Outline platelets.
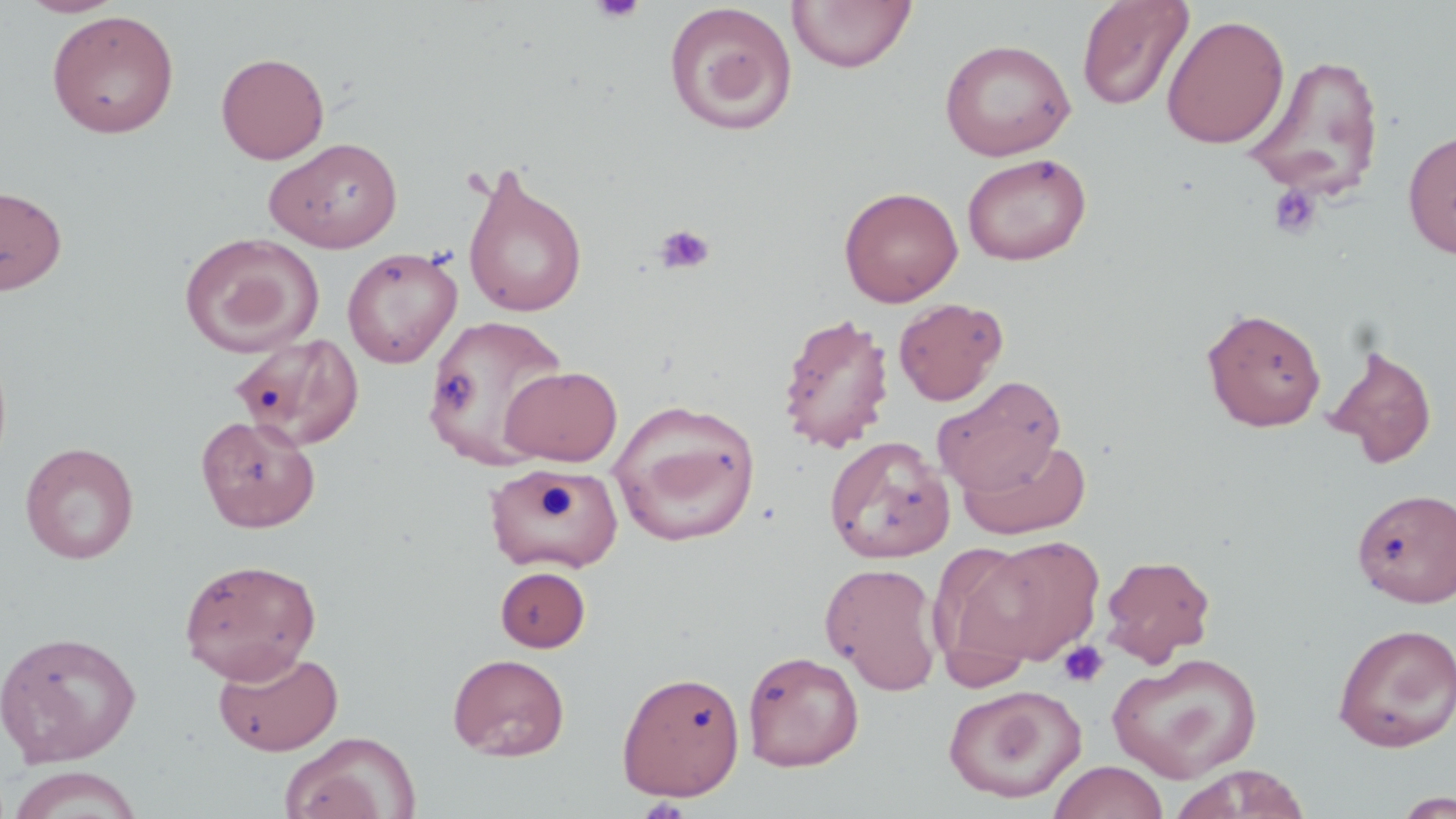

Approximate bounding boxes as [x1, y1, x2, y2] in pixels.
Platelets: [591, 0, 646, 24], [1267, 183, 1323, 240], [653, 223, 715, 275], [1058, 640, 1109, 689].

slide-level diagnosis = no evidence of blood parasites
magnification = 1000x
preparation = thin blood smear
field of view = single
image size = 1456×819 pixels
stain = May-Grünwald-Giemsa
modality = light microscopy
uninfected red blood cell locations = approximate bounding boxes as [x1, y1, x2, y2] in pixels: [16, 0, 126, 18], [1076, 0, 1194, 112], [786, 1, 916, 74], [663, 3, 798, 136], [46, 9, 180, 138], [1162, 14, 1290, 149], [939, 38, 1076, 161], [215, 52, 329, 164], [1245, 52, 1386, 202], [1402, 128, 1456, 260], [264, 137, 403, 253], [962, 152, 1091, 266], [460, 162, 588, 319], [0, 184, 67, 295], [839, 186, 963, 307], [179, 232, 324, 358], [342, 247, 462, 368], [893, 297, 1007, 406], [1200, 307, 1327, 432], [777, 312, 895, 454], [424, 314, 569, 467], [229, 332, 365, 450], [1324, 343, 1438, 469], [499, 365, 623, 466], [932, 376, 1066, 496], [610, 399, 762, 546], [195, 414, 321, 533], [825, 435, 954, 564], [959, 438, 1092, 539], [21, 442, 139, 564], [483, 465, 624, 574], [1353, 487, 1456, 608], [970, 532, 1108, 668], [931, 542, 1060, 680], [1099, 553, 1216, 667], [179, 558, 322, 683], [820, 561, 944, 694], [495, 566, 590, 652], [1332, 623, 1456, 752], [0, 630, 141, 767], [213, 648, 343, 756], [743, 650, 864, 771], [1107, 652, 1263, 784], [447, 653, 570, 761], [616, 670, 746, 801], [943, 684, 1087, 804], [281, 731, 421, 819], [1048, 760, 1169, 819], [1171, 765, 1313, 819], [7, 766, 145, 818], [1388, 791, 1456, 818]